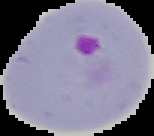
{
  "image_type": "segmented cell region on a black background",
  "malaria_status": "parasitized",
  "preparation": "thin blood smear",
  "image_size": "154×136 pixels"
}